Report the malaria status of this cell.
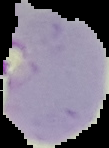
Parasitized.

image_size: 109×148 pixels
preparation: thin blood smear
image_type: segmented cell region on a black background